Assess for parasitized red blood cells.
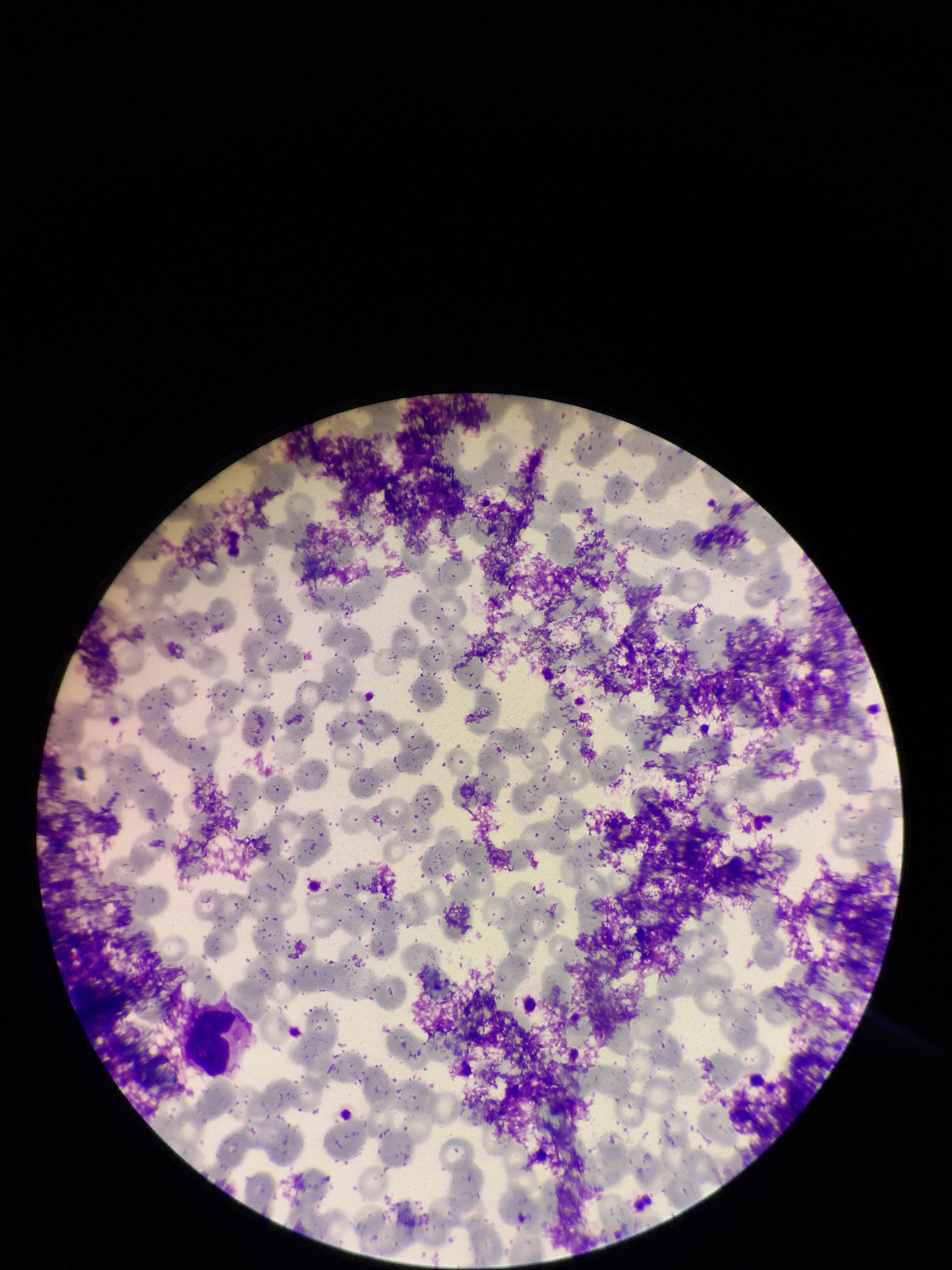
None detected.

One field from this slide. Smartphone photograph taken through the eyepiece of a microscope. Patient malaria status: negative. Image is 952×1270 pixels. Red blood cell count: 258. Giemsa stain. Parasitized red blood cell count: 0. Preparation: thin.